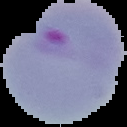

preparation = thin blood smear
image type = cell region segmented out of the field of view; surrounding area masked to black
image size = 127×127 pixels
malaria status = parasitized